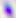
Summary:
  - Identification: Toxoplasma gondii
  - Magnification: 400x
  - Modality: micrograph